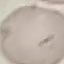

Summary:
  - Result: no malaria parasites seen
  - Stain: Giemsa
  - Image type: automatically extracted cell patch, resized to 64 × 64 pixels
  - Preparation: thin blood smear
  - Capture: smartphone camera at the microscope eyepiece